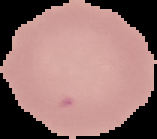
Malaria status: uninfected. Image is 157×139 pixels. From a thin blood film. Cell region segmented out of the field of view; the surrounding area is masked to black.